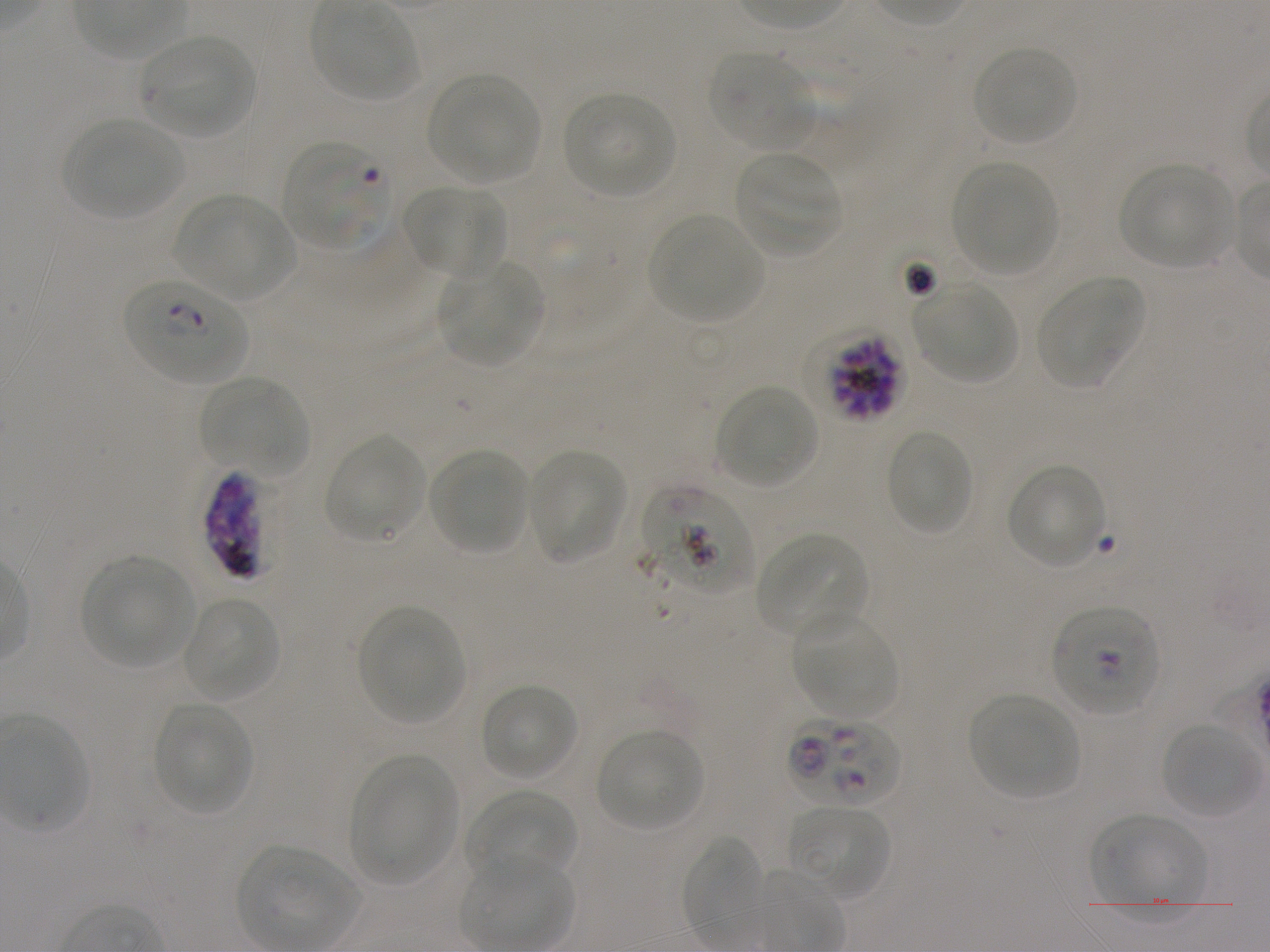
Approximate bounding rectangles given as corner coordinates in pixels from the top-left. Not every red blood cell is marked. A life-cycle stage — or a range of stages, where the recorded stages span more than one — follows each staged infected red blood cell. Locations of infected red blood cells: (x1=123, y1=279, x2=247, y2=383) ring; (x1=803, y1=330, x2=910, y2=424) schizont; (x1=203, y1=470, x2=268, y2=581); (x1=1051, y1=606, x2=1160, y2=714); (x1=788, y1=715, x2=900, y2=807). Locations of uninfected red blood cells: (x1=138, y1=34, x2=255, y2=139), (x1=971, y1=46, x2=1079, y2=147), (x1=708, y1=51, x2=818, y2=151), (x1=428, y1=73, x2=542, y2=184), (x1=563, y1=91, x2=677, y2=198), (x1=63, y1=118, x2=183, y2=220), (x1=735, y1=152, x2=843, y2=259), (x1=951, y1=162, x2=1057, y2=277), (x1=1119, y1=165, x2=1233, y2=269), (x1=402, y1=184, x2=506, y2=280), (x1=175, y1=193, x2=295, y2=301), (x1=648, y1=213, x2=765, y2=322), (x1=438, y1=260, x2=541, y2=367), (x1=1035, y1=277, x2=1145, y2=390), (x1=913, y1=282, x2=1016, y2=382), (x1=198, y1=376, x2=307, y2=476), (x1=715, y1=384, x2=818, y2=488), (x1=886, y1=429, x2=974, y2=536), (x1=323, y1=433, x2=426, y2=544), (x1=428, y1=447, x2=529, y2=555), (x1=526, y1=448, x2=629, y2=565), (x1=1006, y1=463, x2=1110, y2=569), (x1=639, y1=486, x2=754, y2=597), (x1=755, y1=534, x2=869, y2=640), (x1=82, y1=556, x2=196, y2=667), (x1=182, y1=597, x2=279, y2=701), (x1=359, y1=606, x2=465, y2=725), (x1=792, y1=612, x2=900, y2=718), (x1=480, y1=683, x2=578, y2=781), (x1=969, y1=694, x2=1079, y2=799), (x1=153, y1=702, x2=254, y2=815), (x1=1162, y1=721, x2=1261, y2=819), (x1=596, y1=729, x2=704, y2=831), (x1=351, y1=757, x2=458, y2=886), (x1=465, y1=789, x2=579, y2=887), (x1=787, y1=805, x2=891, y2=903), (x1=1089, y1=813, x2=1208, y2=923), (x1=680, y1=834, x2=764, y2=952). Life-cycle stages observed: ring, schizont. Plasmodium falciparum strain NF54 maintained in static in-vitro culture. 100x oil-immersion objective, numerical aperture 1.25. Blood group of the donor: A+. One field from this slide. Giemsa stain. Image is 1270×952 pixels. Thin blood film.